Assess for Plasmodium parasites.
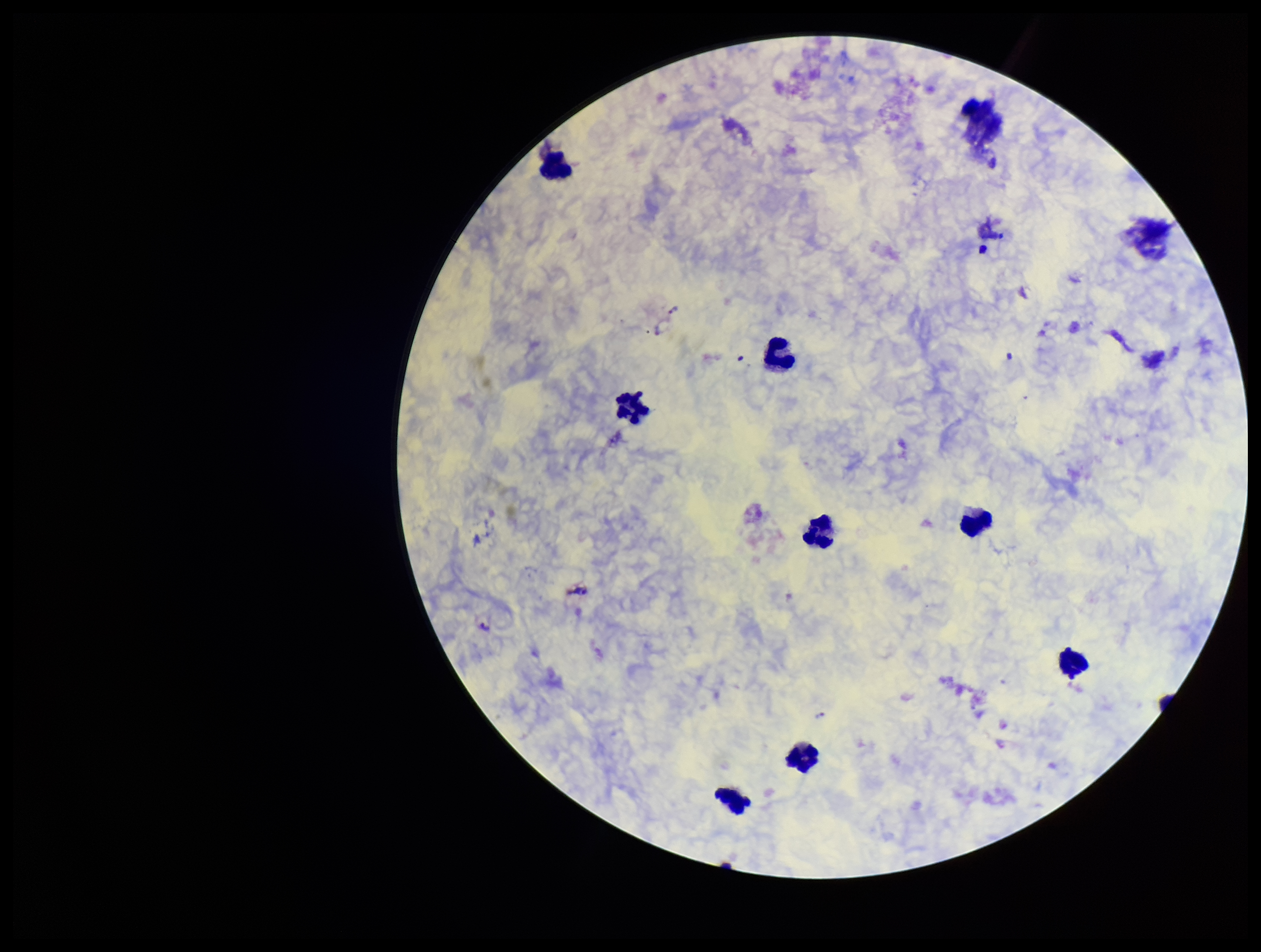

None detected.

Summary:
  - Image size: 1261×952 pixels
  - Leukocyte count: 10
  - Patient malaria status: positive
  - Parasite count: 0
  - Field of view: one from this slide
  - Species reported for this patient: Plasmodium vivax
  - Capture: smartphone photograph through the microscope eyepiece
  - Stain: Giemsa
  - Preparation: thick